Classify this cell by malaria status.
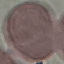

Uninfected.

stain = Giemsa
capture = smartphone through the microscope eyepiece
image type = automatically extracted cell patch, resized to 64 × 64 pixels
preparation = thin smear